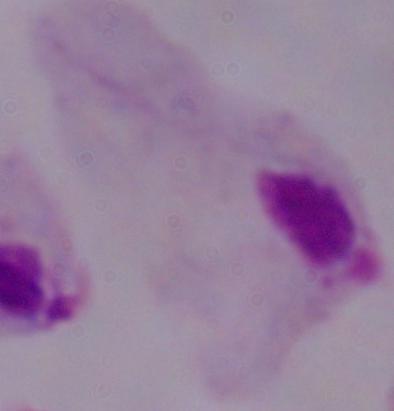
magnification: 1000x
identification: trichomonad
modality: photomicrograph